State which parasite is depicted.
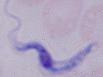
This is a trypanosome.

modality = photomicrograph
magnification = 1000x